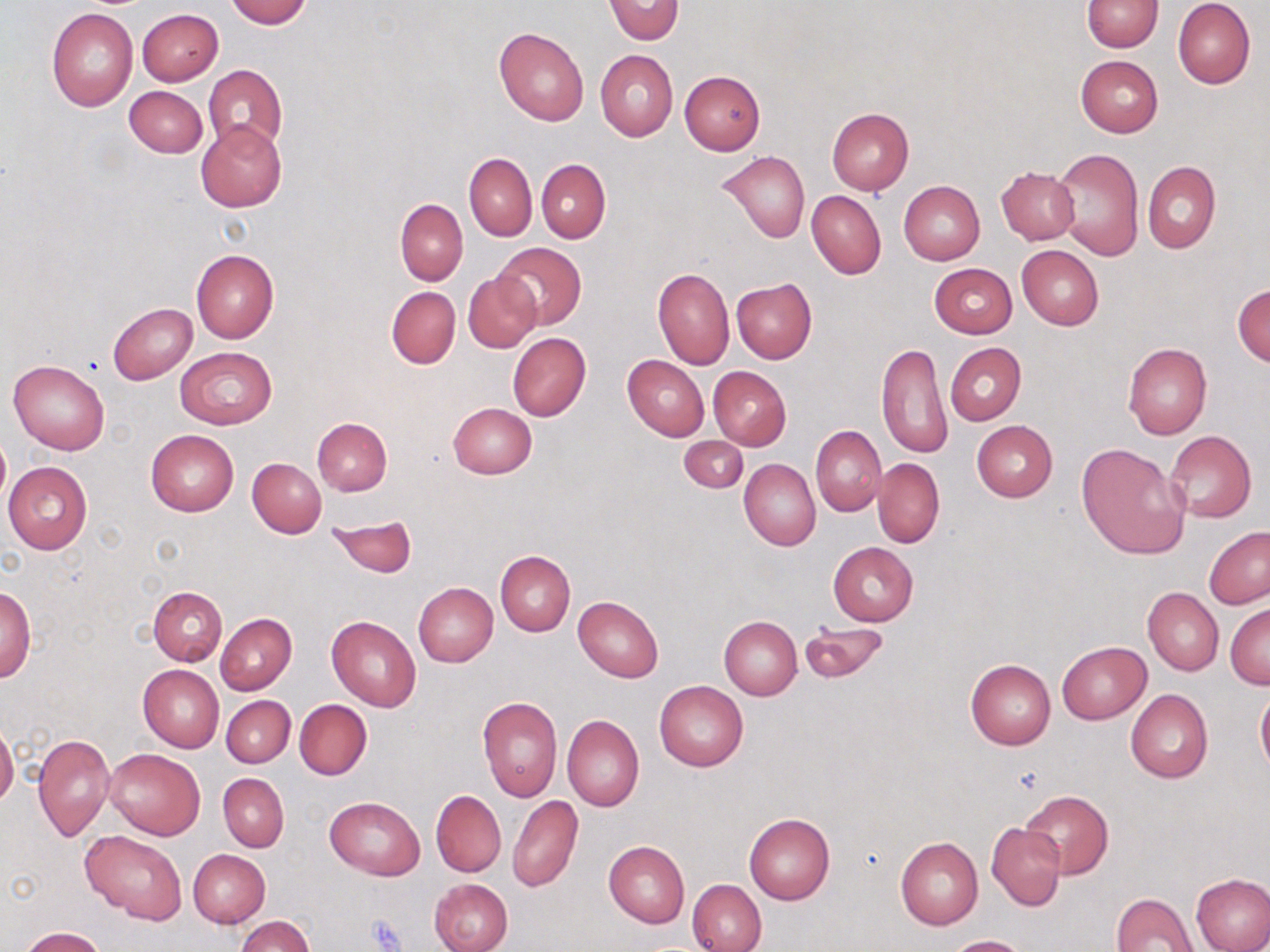
{
  "slide_level_diagnosis": "no evidence of blood parasites",
  "uninfected_red_blood_cell_locations": "approximate bounding boxes as named x1/y1/x2/y2 corners in pixels: (x1=225, y1=0, x2=311, y2=27), (x1=604, y1=0, x2=683, y2=45), (x1=1082, y1=0, x2=1162, y2=52), (x1=1172, y1=0, x2=1255, y2=89), (x1=46, y1=7, x2=138, y2=110), (x1=137, y1=8, x2=223, y2=85), (x1=133, y1=10, x2=214, y2=160), (x1=494, y1=26, x2=589, y2=126), (x1=595, y1=50, x2=678, y2=140), (x1=1075, y1=55, x2=1163, y2=138), (x1=203, y1=64, x2=288, y2=154), (x1=679, y1=71, x2=765, y2=156), (x1=124, y1=86, x2=207, y2=157), (x1=826, y1=108, x2=913, y2=195), (x1=195, y1=120, x2=287, y2=212), (x1=1052, y1=148, x2=1144, y2=261), (x1=719, y1=150, x2=809, y2=243), (x1=464, y1=152, x2=537, y2=241), (x1=536, y1=160, x2=610, y2=243), (x1=1143, y1=161, x2=1220, y2=254), (x1=995, y1=167, x2=1079, y2=245), (x1=897, y1=180, x2=984, y2=266), (x1=807, y1=190, x2=886, y2=279), (x1=396, y1=199, x2=467, y2=285), (x1=492, y1=242, x2=587, y2=328), (x1=1016, y1=245, x2=1104, y2=329), (x1=191, y1=250, x2=278, y2=343), (x1=930, y1=263, x2=1017, y2=338), (x1=653, y1=268, x2=734, y2=369), (x1=462, y1=272, x2=542, y2=353), (x1=732, y1=279, x2=816, y2=363), (x1=1233, y1=283, x2=1270, y2=365), (x1=386, y1=286, x2=461, y2=369), (x1=107, y1=303, x2=197, y2=384), (x1=507, y1=333, x2=591, y2=421), (x1=876, y1=342, x2=954, y2=460), (x1=1122, y1=342, x2=1212, y2=440), (x1=946, y1=343, x2=1025, y2=425), (x1=174, y1=345, x2=278, y2=430), (x1=622, y1=355, x2=709, y2=440), (x1=8, y1=360, x2=110, y2=454), (x1=708, y1=366, x2=791, y2=450), (x1=447, y1=402, x2=538, y2=479), (x1=312, y1=417, x2=392, y2=496), (x1=972, y1=421, x2=1057, y2=501), (x1=811, y1=426, x2=887, y2=516), (x1=146, y1=429, x2=238, y2=516), (x1=1165, y1=430, x2=1256, y2=523), (x1=0, y1=432, x2=10, y2=509), (x1=679, y1=435, x2=749, y2=493), (x1=1077, y1=442, x2=1190, y2=559), (x1=248, y1=458, x2=325, y2=537), (x1=873, y1=458, x2=945, y2=549), (x1=739, y1=459, x2=820, y2=550), (x1=3, y1=462, x2=92, y2=553), (x1=327, y1=515, x2=416, y2=576), (x1=1204, y1=526, x2=1270, y2=609), (x1=828, y1=542, x2=919, y2=625), (x1=495, y1=550, x2=575, y2=635), (x1=414, y1=583, x2=498, y2=667), (x1=1, y1=585, x2=36, y2=683), (x1=148, y1=586, x2=227, y2=666), (x1=1143, y1=588, x2=1223, y2=675), (x1=573, y1=595, x2=664, y2=683), (x1=1226, y1=603, x2=1269, y2=689), (x1=216, y1=614, x2=296, y2=694), (x1=327, y1=616, x2=422, y2=712), (x1=718, y1=617, x2=802, y2=699), (x1=801, y1=619, x2=889, y2=685), (x1=1056, y1=641, x2=1152, y2=724), (x1=965, y1=659, x2=1056, y2=749), (x1=138, y1=664, x2=224, y2=752), (x1=655, y1=680, x2=749, y2=771), (x1=1125, y1=688, x2=1213, y2=783), (x1=1255, y1=689, x2=1270, y2=774), (x1=222, y1=696, x2=295, y2=767), (x1=478, y1=697, x2=563, y2=801), (x1=294, y1=700, x2=371, y2=780), (x1=561, y1=716, x2=644, y2=811), (x1=0, y1=724, x2=18, y2=806), (x1=33, y1=733, x2=115, y2=843), (x1=104, y1=748, x2=205, y2=840), (x1=219, y1=774, x2=289, y2=852), (x1=431, y1=789, x2=506, y2=878), (x1=1021, y1=790, x2=1113, y2=879), (x1=325, y1=795, x2=426, y2=880), (x1=508, y1=796, x2=582, y2=893), (x1=743, y1=813, x2=835, y2=905), (x1=986, y1=822, x2=1066, y2=910), (x1=81, y1=830, x2=187, y2=924), (x1=896, y1=838, x2=983, y2=930), (x1=604, y1=840, x2=689, y2=927), (x1=188, y1=849, x2=270, y2=927), (x1=1191, y1=872, x2=1270, y2=952), (x1=429, y1=878, x2=512, y2=952), (x1=687, y1=878, x2=766, y2=952), (x1=1112, y1=891, x2=1199, y2=952), (x1=237, y1=916, x2=314, y2=952), (x1=19, y1=927, x2=105, y2=951), (x1=944, y1=935, x2=1031, y2=952)",
  "modality": "light microscopy",
  "platelet_locations": "approximate bounding boxes as named x1/y1/x2/y2 corners in pixels: (x1=367, y1=916, x2=406, y2=951)",
  "magnification": "1000x",
  "field_of_view": "single",
  "stain": "May-Grünwald-Giemsa",
  "preparation": "thin blood smear",
  "image_size": "1270×952 pixels"
}